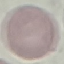
malaria status = uninfected
stain = Giemsa
capture = smartphone camera at the microscope eyepiece
preparation = thin blood film
image type = cell patch, automatically extracted from a larger field of view and resized to 64 × 64 pixels